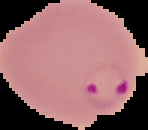
The area outside the segmented cell region is set to black. Image is 148×130 pixels. Result: Plasmodium parasites identified. From a thin blood smear.